Outline each blood parasite and name the species.
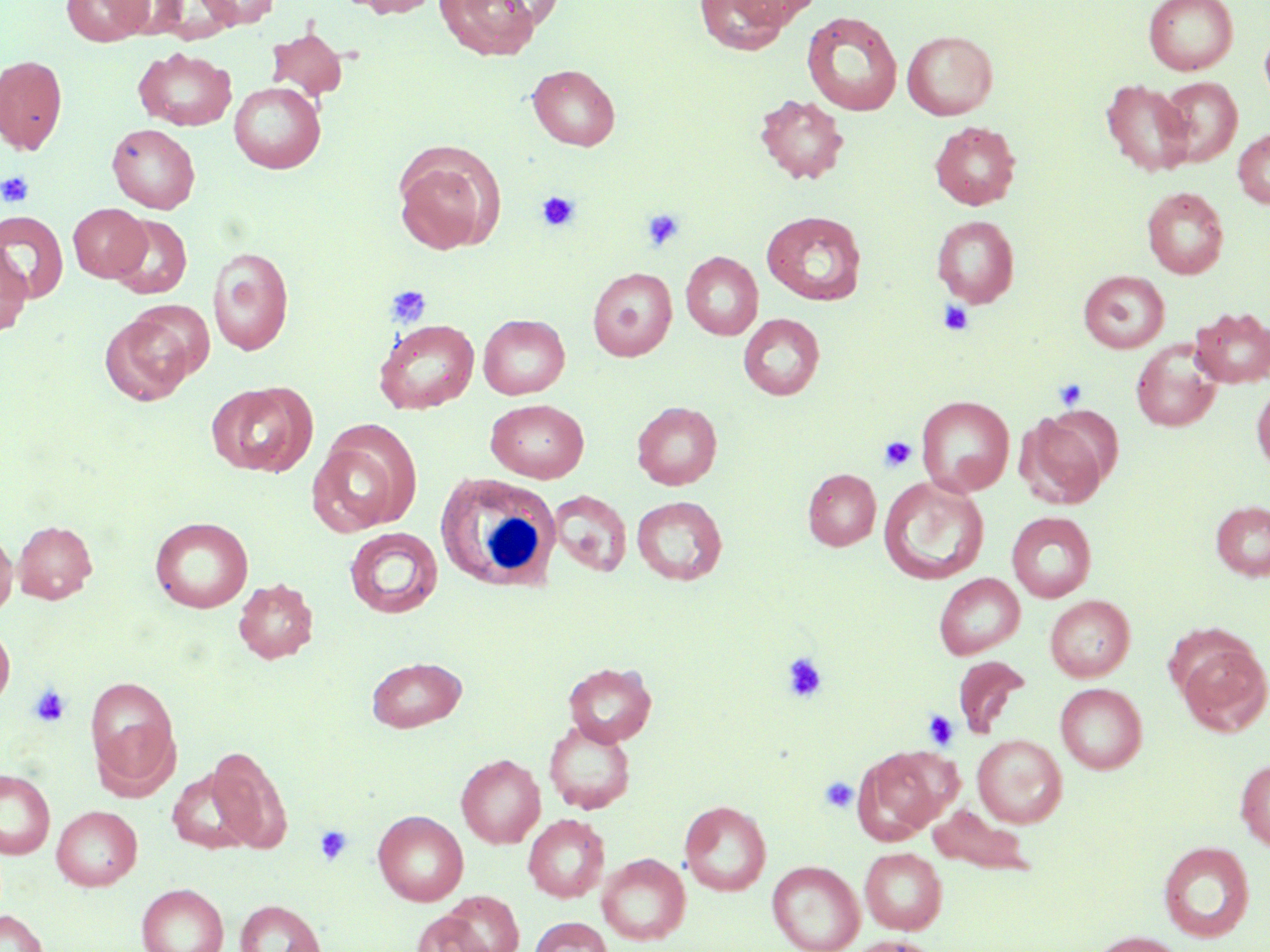

No blood parasites seen.

Summary:
  - Coordinate format: approximate bounding boxes as [x1, y1, x2, y2] in pixels
  - White blood cell locations: [435, 471, 563, 594]
  - Uninfected red blood cell locations: [62, 0, 151, 46], [106, 0, 190, 39], [193, 0, 279, 29], [349, 0, 440, 18], [435, 0, 541, 60], [481, 0, 566, 28], [693, 0, 793, 55], [727, 0, 823, 27], [1143, 0, 1238, 75], [801, 10, 902, 116], [266, 27, 348, 102], [1259, 27, 1270, 107], [902, 30, 998, 120], [134, 47, 237, 131], [0, 54, 68, 155], [527, 64, 621, 150], [1158, 77, 1243, 166], [1101, 79, 1194, 177], [229, 81, 326, 173], [755, 93, 848, 183], [930, 121, 1021, 209], [107, 123, 200, 213], [1233, 129, 1270, 208], [392, 142, 502, 255], [1142, 187, 1228, 279], [68, 203, 151, 281], [0, 210, 68, 303], [761, 210, 867, 305], [109, 214, 192, 299], [931, 215, 1020, 308], [207, 247, 295, 355], [0, 248, 32, 336], [681, 251, 763, 340], [587, 267, 677, 361], [1079, 270, 1169, 353], [1190, 307, 1270, 388], [99, 312, 196, 406], [478, 314, 570, 399], [738, 314, 825, 400], [373, 319, 478, 413], [1131, 340, 1221, 432], [206, 381, 315, 477], [1251, 384, 1270, 474], [916, 395, 1015, 496], [485, 399, 589, 483], [632, 401, 722, 489], [1017, 410, 1114, 509], [307, 426, 420, 536], [802, 468, 881, 551], [879, 477, 989, 584], [548, 490, 632, 576], [632, 496, 727, 585], [1210, 500, 1270, 581], [1007, 512, 1097, 603], [150, 516, 253, 612], [13, 520, 98, 604], [344, 527, 443, 618], [0, 528, 17, 619], [934, 573, 1025, 659], [233, 577, 318, 663], [1045, 595, 1135, 682], [0, 621, 15, 712], [1175, 636, 1270, 736], [366, 656, 466, 732], [952, 656, 1030, 737], [563, 662, 657, 747], [85, 675, 180, 789], [1055, 683, 1147, 773], [544, 719, 636, 814], [972, 734, 1067, 827], [206, 745, 293, 853], [855, 747, 952, 842], [456, 754, 545, 848], [1235, 758, 1270, 851], [167, 768, 257, 852], [0, 769, 55, 858], [679, 800, 771, 896], [928, 804, 1035, 876], [52, 805, 142, 890], [373, 810, 469, 906], [523, 814, 610, 902], [1158, 840, 1255, 942], [859, 848, 947, 934], [597, 853, 690, 945], [768, 860, 864, 952], [137, 884, 227, 952], [440, 891, 524, 952], [235, 899, 326, 952], [0, 910, 47, 952], [411, 911, 492, 952], [528, 917, 613, 952], [1086, 931, 1191, 952], [842, 936, 937, 952]
  - Platelet locations: [0, 171, 34, 208], [536, 190, 580, 233], [642, 208, 686, 251], [385, 284, 431, 329], [937, 300, 974, 337], [1053, 377, 1089, 411], [879, 436, 917, 472], [781, 652, 828, 702], [29, 684, 71, 727], [923, 710, 959, 750], [819, 776, 858, 813], [314, 825, 353, 866]
  - Slide-level diagnosis: negative for blood parasites
  - Preparation: thin blood smear
  - Image size: 1270×952 pixels
  - Modality: optical microscopy
  - Magnification: 1000x
  - Field of view: one of a larger specimen
  - Stain: May-Grünwald-Giemsa